Report the malaria status of this cell.
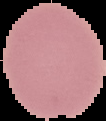

Uninfected.

{
  "image_size": "106×121 pixels",
  "preparation": "thin blood film",
  "image_type": "segmented cell region on a black background"
}